Evaluate for Plasmodium parasites.
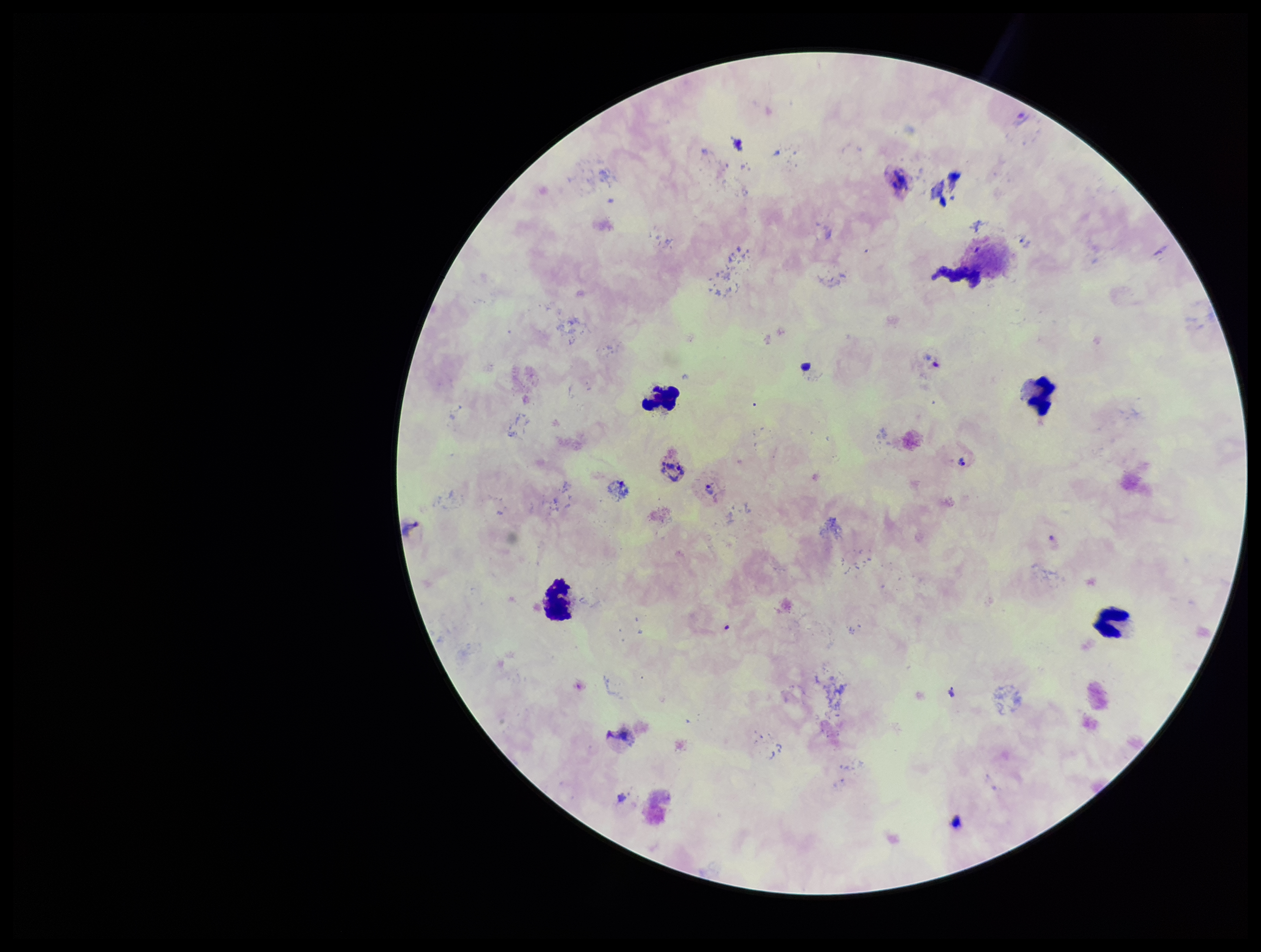

Identified.

Patient malaria status: positive. Giemsa stain. Parasite count: 5. Single field of view. Leukocyte count: 5. Species reported for this patient: Plasmodium vivax. Image is 1261×952 pixels. Preparation: thick smear. Smartphone photograph taken through the eyepiece of a microscope.